Assess this cell for malaria.
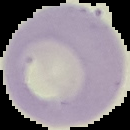

Uninfected.

Summary:
  - Image size: 130×130 pixels
  - Preparation: thin blood smear
  - Image type: segmented cell region on a black background